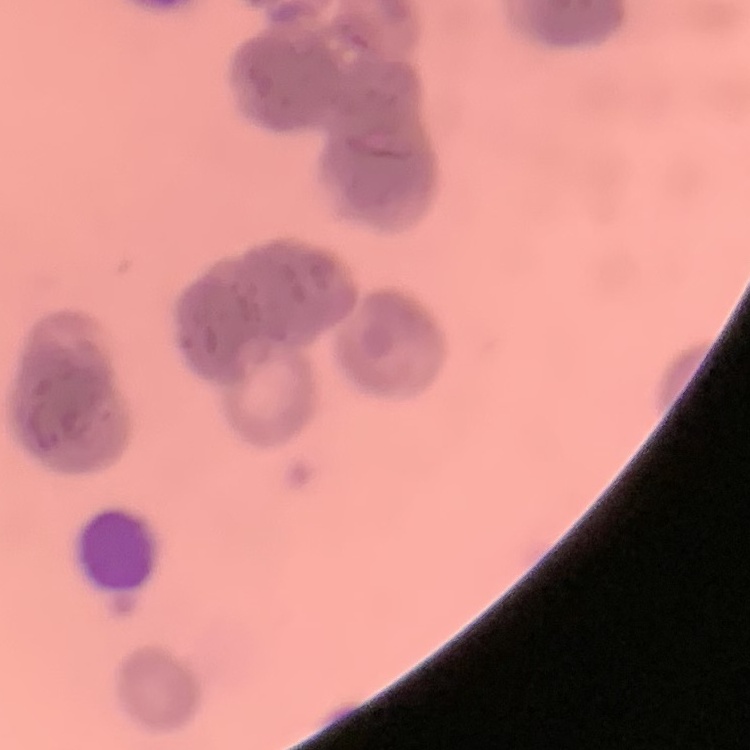
Summary:
  - Red blood cell morphology: rouleaux formation
  - Preparation: thin blood smear
  - Image type: square crop of a larger photomicrograph
  - Stain: Field's or Giemsa